Assess this cell for malaria.
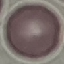
Uninfected.

Giemsa stain. Thin blood film. Acquired by smartphone through the microscope eyepiece. Cell patch, automatically extracted from a larger field of view and resized to 64 × 64 pixels.